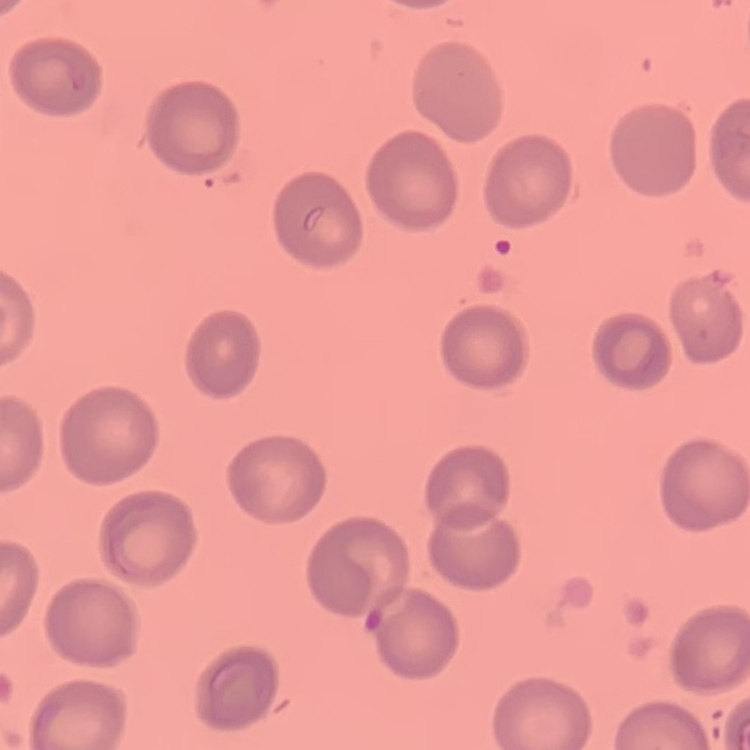

Summary:
  - Red blood cell morphology: no rouleaux formation
  - Stain: Field's or Giemsa
  - Preparation: thin blood film
  - Image type: square crop of a larger photomicrograph